Outline every parasitised red blood cell.
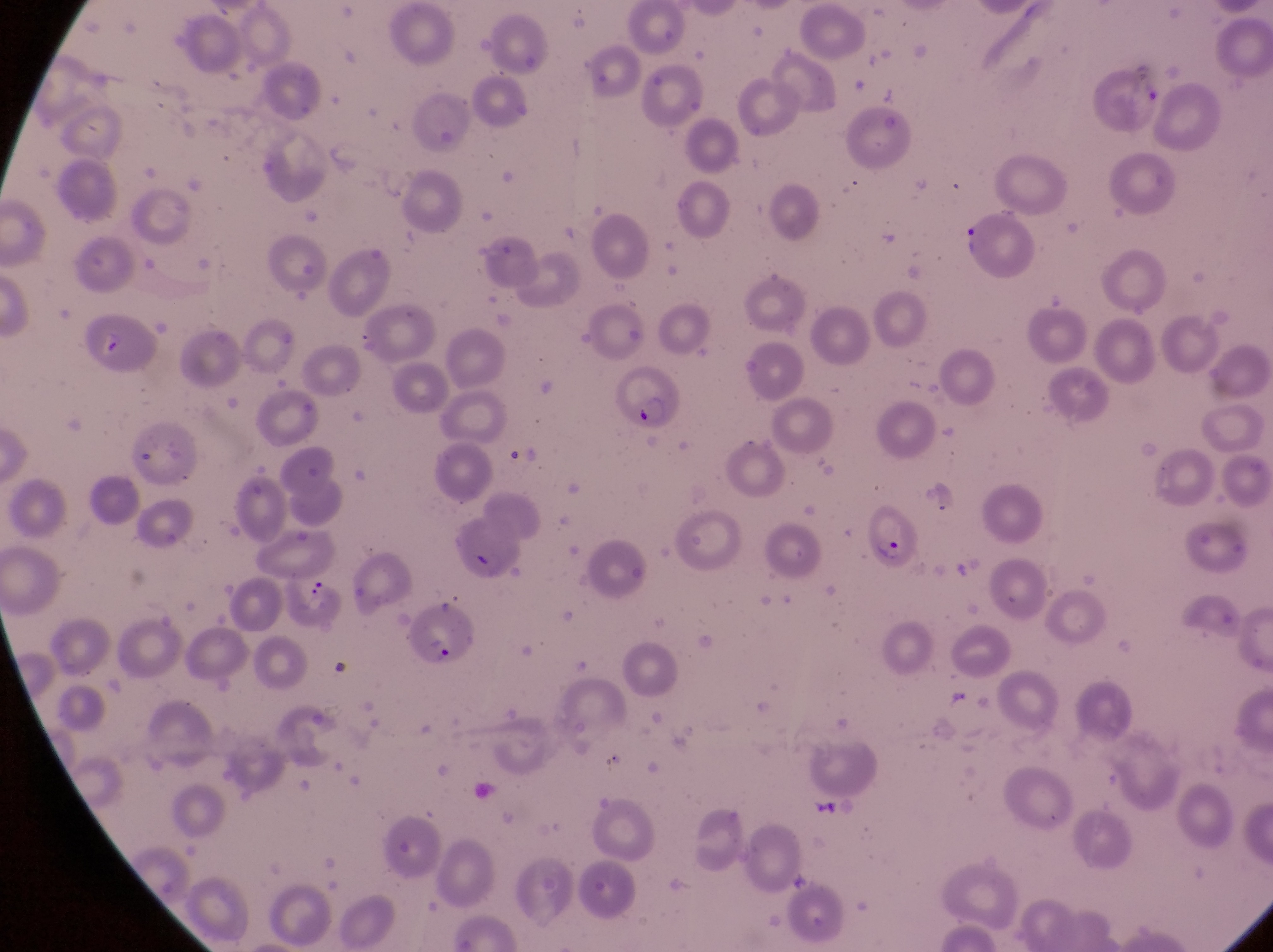
Approximate bounding boxes as left top right bottom in pixels.
Parasitised red blood cells: 604 370 684 433; 859 507 929 577; 405 597 485 671.

Summary:
  - Country: Uganda
  - Image size: 1273×952 pixels
  - Field of view: single
  - Magnification: 1000x
  - Capture: smartphone photograph through the eyepiece of an Olympus CX-23 microscope
  - Preparation: thin blood smear